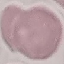

Summary:
  - Malaria status: uninfected
  - Image type: cell patch, automatically extracted from a larger field of view and resized to 64 × 64 pixels
  - Stain: Giemsa
  - Capture: smartphone through the microscope eyepiece
  - Preparation: thin blood film